State the preparation type.
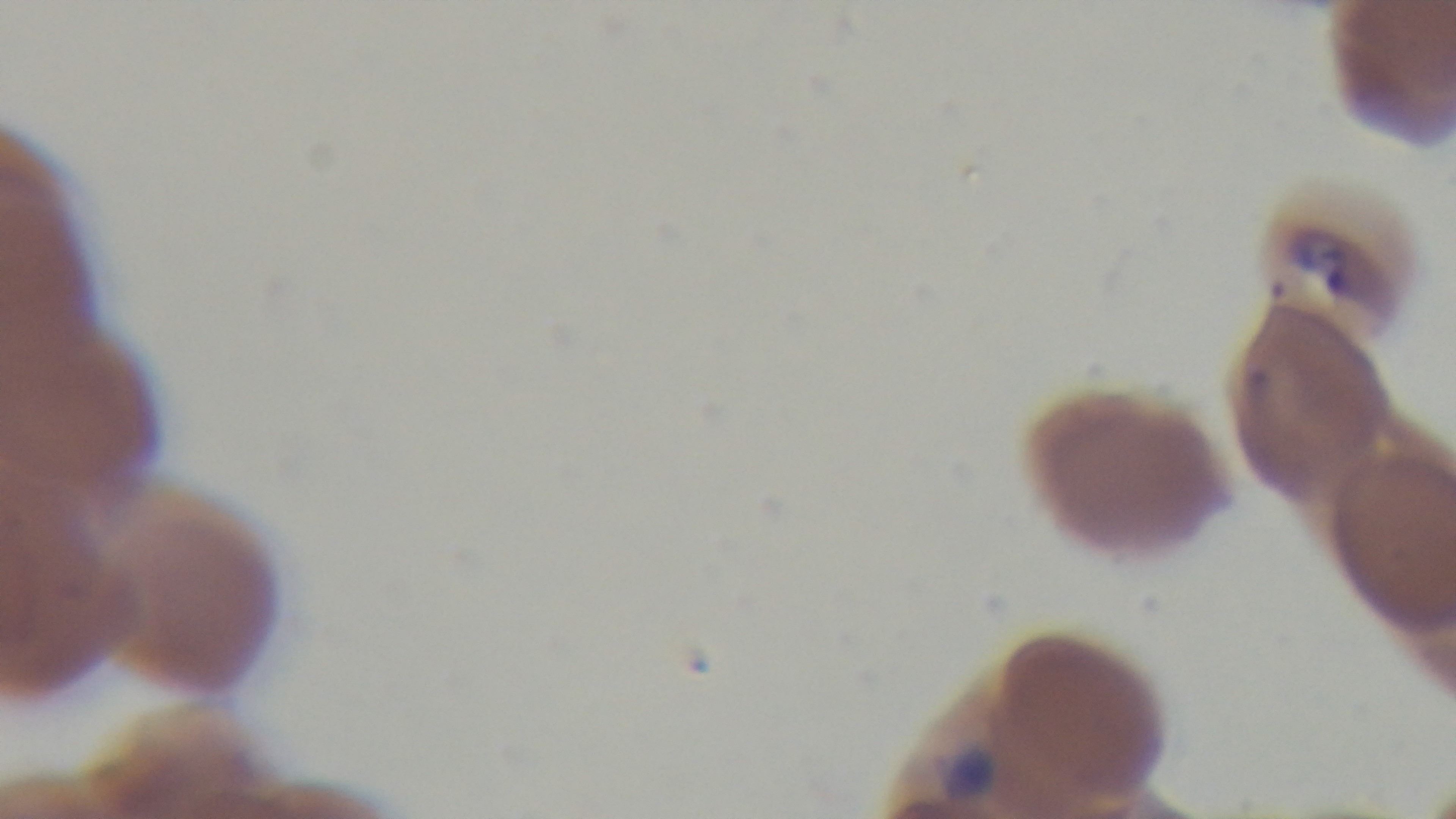
It is a thin blood film.

capture = mounted 4K digital camera
stain = Giemsa
field of view = single
malaria status = positive
modality = light microscopy
objective = 100x oil immersion